Report the malaria status of this cell.
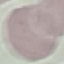
It is uninfected.

{
  "stain": "Giemsa",
  "capture": "smartphone camera at the microscope eyepiece",
  "preparation": "thin smear",
  "image_type": "cell patch, automatically extracted from a larger field of view and resized to 64 × 64 pixels"
}